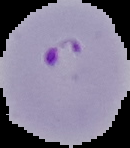
result = malaria parasites detected
preparation = thin blood film
image size = 130×148 pixels
image type = segmented cell region with the area outside set to black